Identify the parasite.
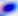

This is Toxoplasma gondii.

400x magnification. Photomicrograph.